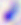
Summary:
  - Modality: micrograph
  - Identification: Toxoplasma gondii
  - Magnification: 400x